Name the cell type shown.
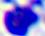
This is a leukocyte.

modality = photomicrograph
magnification = 400x